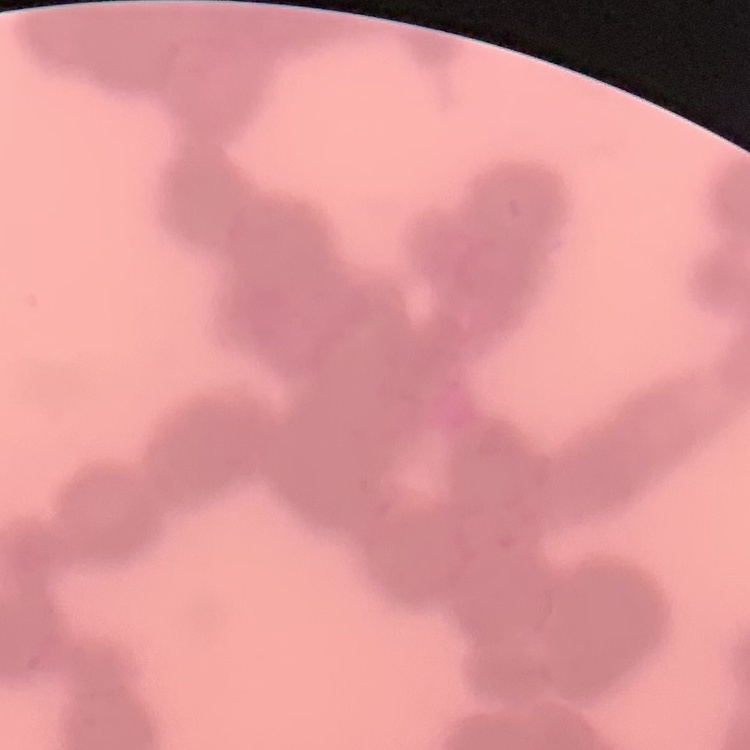

red blood cell morphology = rouleaux formation
image type = square crop of a larger photomicrograph
stain = Field's or Giemsa
preparation = thin blood smear